Describe the morphology of the red blood cells.
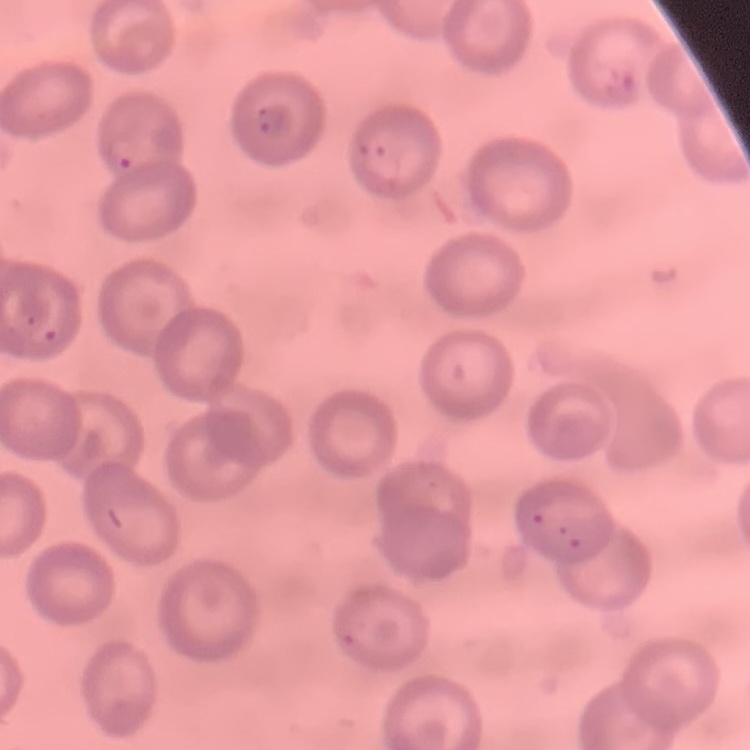

They show no rouleaux formation.

Summary:
  - Preparation: thin blood film
  - Stain: Field's or Giemsa
  - Image type: one tile cut from a larger photomicrograph